Report the malaria status of this cell.
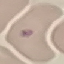

Uninfected.

Summary:
  - Image type: automatically extracted cell patch, resized to 64 × 64 pixels
  - Capture: smartphone through the microscope eyepiece
  - Preparation: thin blood smear
  - Stain: Giemsa